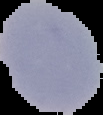
Result: no Plasmodium parasites seen. Cell region segmented out of the field of view; the surrounding area is masked to black. From a thin blood smear. Image is 103×115 pixels.